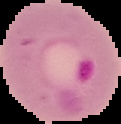

Summary:
  - Image size: 121×124 pixels
  - Image type: segmented cell region with the area outside set to black
  - Malaria status: parasitized
  - Preparation: thin blood smear